Outline each blood parasite and name the species.
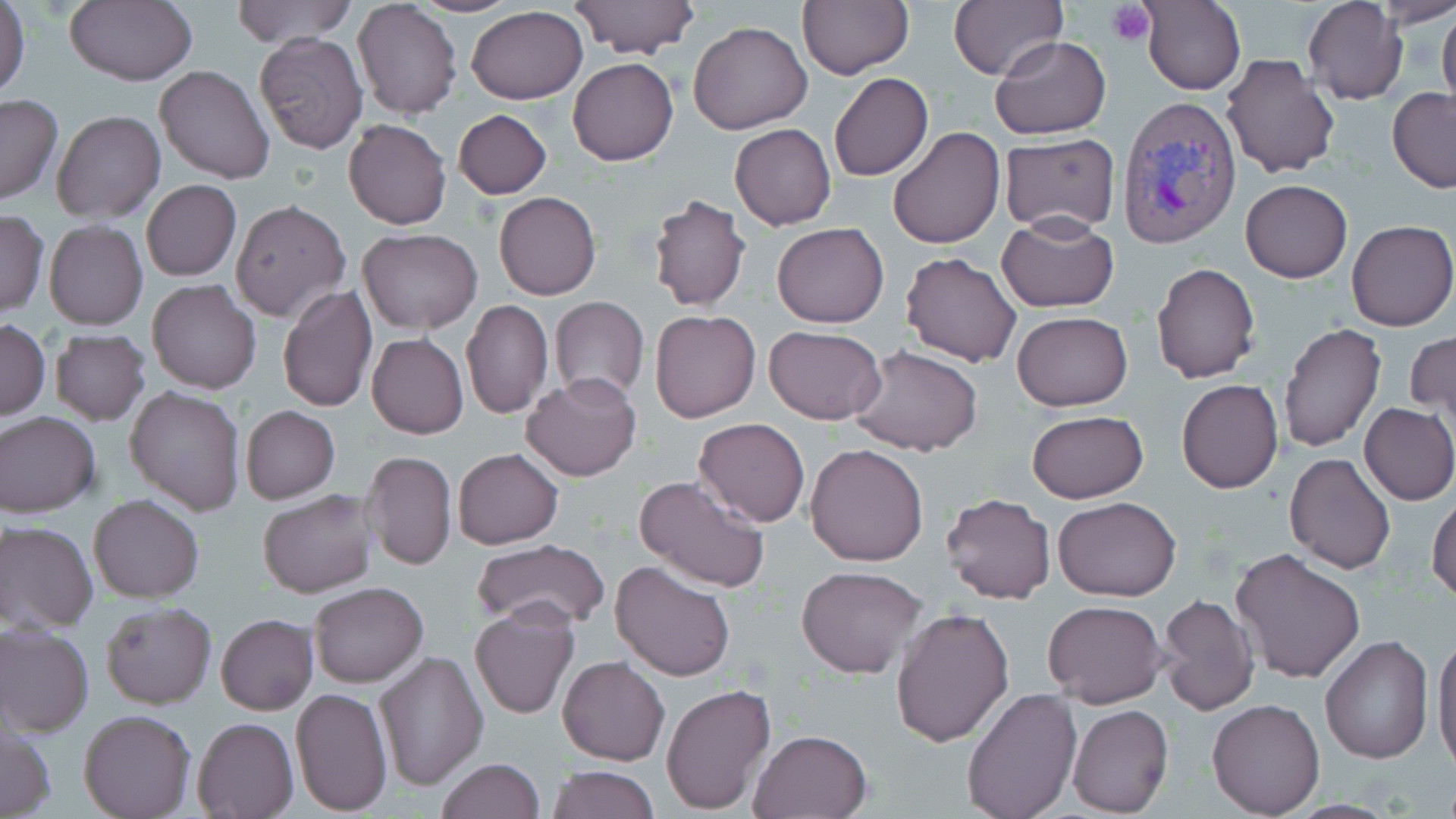
Approximate bounding boxes as (x1, y1, x2, y2) in pixels.
Plasmodium vivax-infected red blood cells: (1116, 95, 1242, 251).
No Plasmodium falciparum, Plasmodium ovale, Plasmodium malariae, Babesia divergens, or Trypanosoma brucei observed.

Summary:
  - Uninfected red blood cell locations: (229, 0, 358, 48), (408, 0, 520, 18), (569, 0, 699, 59), (796, 0, 913, 80), (1304, 0, 1408, 105), (1374, 0, 1456, 28), (0, 1, 29, 102), (64, 1, 198, 87), (353, 1, 462, 119), (949, 1, 1064, 80), (1142, 1, 1246, 96), (1437, 5, 1456, 119), (466, 6, 588, 104), (688, 21, 812, 134), (253, 31, 369, 155), (988, 33, 1112, 139), (1221, 52, 1340, 176), (568, 58, 678, 166), (154, 65, 275, 184), (828, 71, 933, 182), (1387, 88, 1456, 193), (0, 94, 63, 205), (453, 109, 552, 199), (51, 110, 165, 225), (343, 119, 451, 230), (730, 123, 836, 230), (885, 125, 1005, 248), (999, 134, 1120, 234), (1240, 179, 1351, 282), (142, 180, 240, 281), (494, 191, 601, 300), (647, 193, 752, 313), (230, 200, 350, 322), (0, 209, 50, 318), (998, 215, 1119, 313), (45, 220, 147, 330), (1347, 220, 1456, 332), (772, 222, 889, 329), (357, 227, 482, 335), (900, 251, 1022, 367), (1151, 262, 1261, 384), (147, 280, 260, 393), (277, 284, 377, 412), (548, 296, 649, 401), (460, 299, 553, 418), (649, 309, 759, 422), (1012, 311, 1132, 412), (0, 319, 50, 421), (1277, 323, 1386, 455), (763, 325, 887, 424), (50, 329, 150, 425), (1406, 331, 1456, 421), (366, 333, 469, 440), (850, 346, 984, 456), (522, 375, 641, 482), (1175, 378, 1285, 494), (125, 385, 245, 516), (1359, 402, 1455, 505), (240, 405, 341, 505), (1026, 410, 1150, 504), (0, 412, 101, 518), (693, 417, 810, 526), (805, 443, 930, 566), (453, 447, 563, 550), (362, 450, 456, 571), (1284, 453, 1395, 573), (634, 473, 771, 592), (257, 489, 379, 598), (941, 492, 1056, 604), (1429, 494, 1456, 603), (88, 495, 205, 603), (1052, 496, 1181, 602), (1, 520, 98, 633), (472, 540, 611, 632), (1230, 548, 1367, 684), (610, 559, 737, 682), (797, 566, 929, 679), (309, 580, 428, 687), (1156, 595, 1260, 716), (212, 597, 427, 701), (1043, 600, 1166, 708), (101, 602, 216, 709), (470, 603, 579, 720), (890, 606, 1015, 747), (216, 614, 318, 715), (0, 623, 94, 736), (1431, 630, 1455, 770), (1319, 635, 1434, 764), (372, 650, 489, 790), (557, 655, 670, 766), (661, 684, 776, 813), (960, 687, 1083, 819), (290, 688, 392, 816), (1207, 698, 1325, 817), (1067, 705, 1174, 817), (78, 708, 196, 819), (192, 717, 299, 818), (0, 722, 55, 818), (747, 728, 874, 818), (434, 758, 544, 819), (546, 764, 659, 819)
  - Platelet locations: (1109, 1, 1156, 48)
  - Slide-level diagnosis: Plasmodium vivax
  - Stain: May-Grünwald-Giemsa
  - Modality: light microscopy
  - Magnification: 1000x
  - Image size: 1456×819 pixels
  - Preparation: thin blood smear
  - Field of view: single